Classify this cell by malaria status.
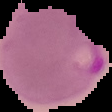

Parasitized.

Summary:
  - Image size: 112×112 pixels
  - Preparation: thin blood film
  - Image type: segmented cell region on a black background